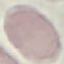

Malaria status: uninfected. Giemsa stain. Photographed with a smartphone camera at the microscope eyepiece. Cell patch, automatically extracted from a larger field of view and resized to 64 × 64 pixels. Thin blood smear.